Assess this cell for malaria.
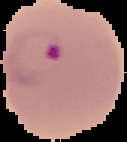

Parasitized.

Image is 127×142 pixels. Segmented cell region on a black background. From a thin blood film.